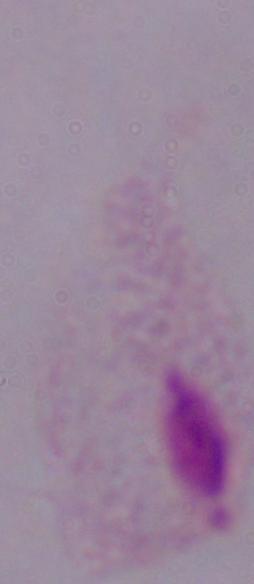
{
  "modality": "micrograph",
  "magnification": "1000x",
  "identification": "trichomonad"
}